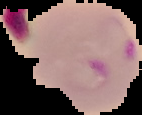

Summary:
  - Image type: segmented cell region with the area outside set to black
  - Result: Plasmodium parasites identified
  - Image size: 142×115 pixels
  - Preparation: thin blood smear